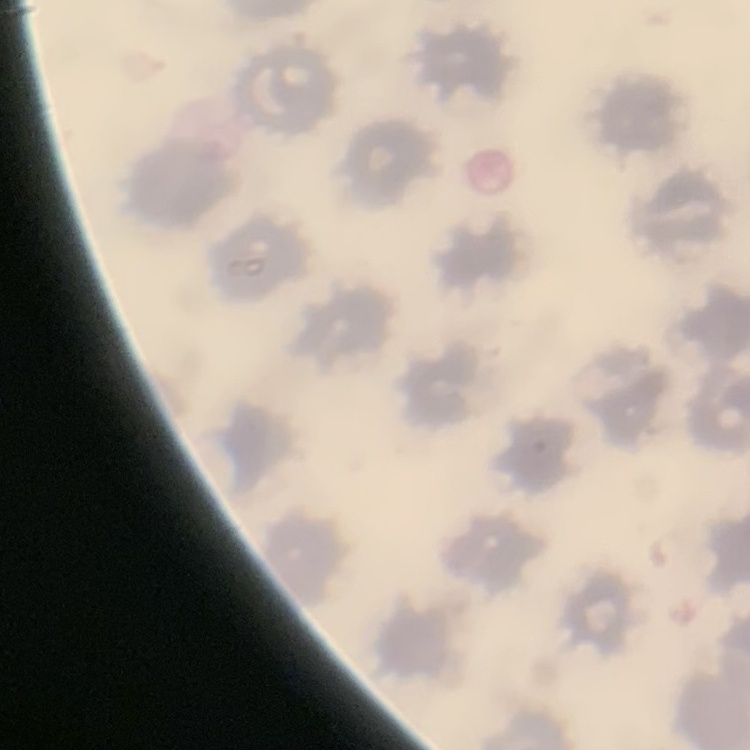

Summary:
  - Red blood cell morphology: no rouleaux formation
  - Image type: square crop of a larger photomicrograph
  - Stain: Field's or Giemsa
  - Preparation: thin blood film